State the preparation type.
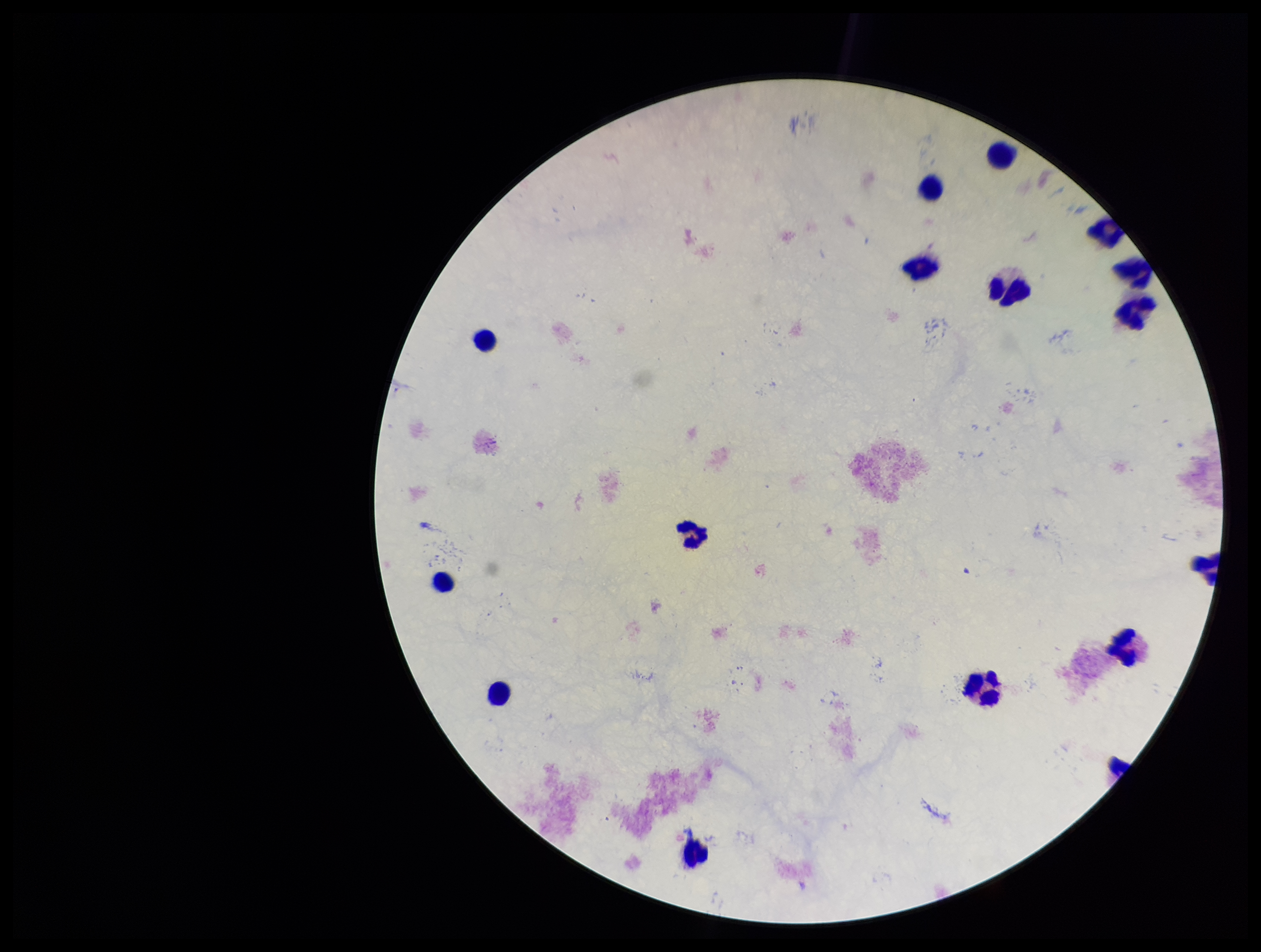
It is a thick blood smear.

{
  "stain": "Giemsa",
  "plasmodium_parasites": "none seen",
  "leukocyte_count": 15,
  "capture": "smartphone photograph through the microscope eyepiece",
  "parasite_count": 0,
  "patient_malaria_status": "negative",
  "field_of_view": "single",
  "image_size": "1261×952 pixels"
}